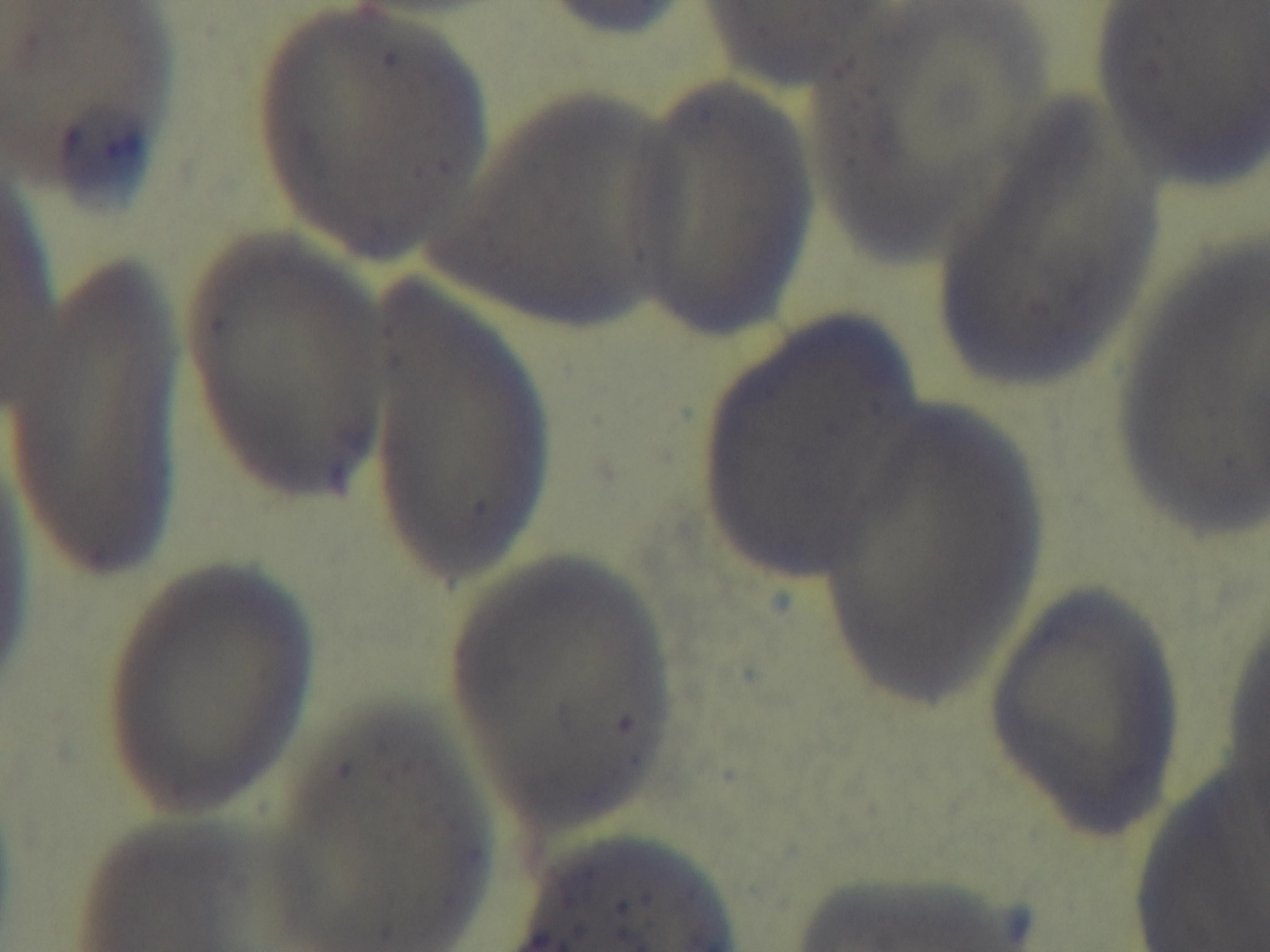 Giemsa stain. Malaria status: negative. Photomicrograph. Preparation: thin. One field from the slide. 100x oil-immersion objective. Mounted 4K digital camera.